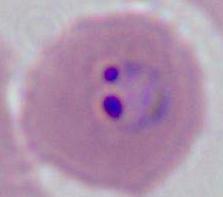

identification: Plasmodium
modality: photomicrograph
magnification: 400x or 1000x